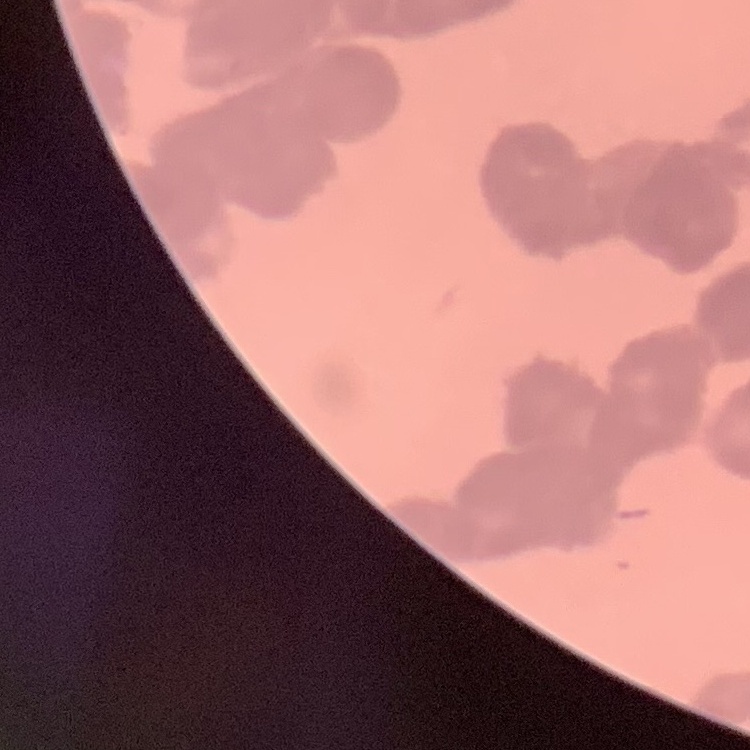
The red blood cells show rouleaux formation. Thin blood film. Field's or Giemsa stain. Square crop of a larger photomicrograph.